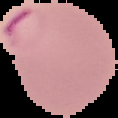

Malaria status: parasitized. The area outside the segmented cell region is set to black. Image is 118×118 pixels. From a thin blood film.